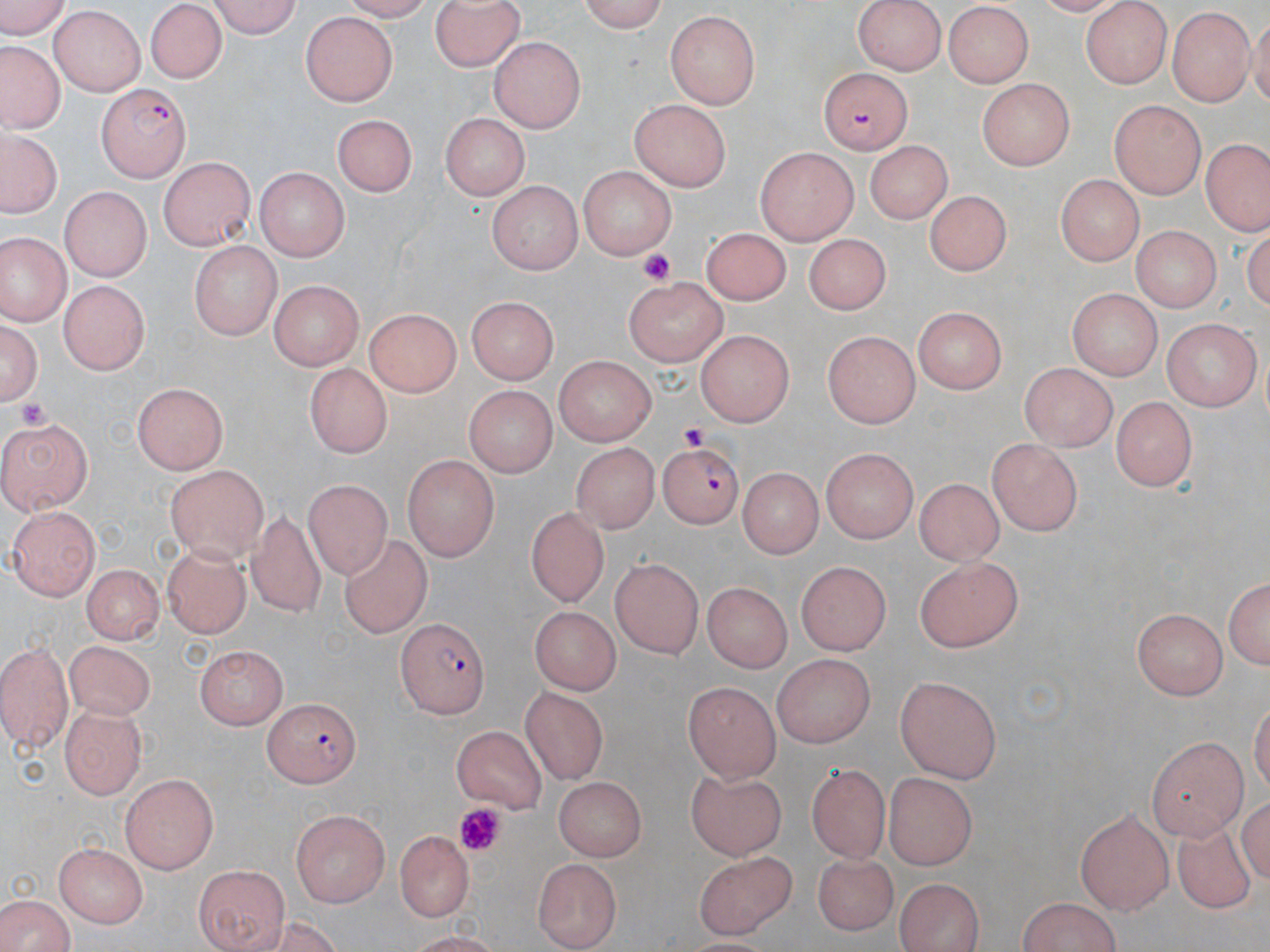
Approximate bounding boxes as (x1,y1)-(x2,y2) corner pairs in pixels. Plasmodium falciparum-infected red blood cell locations: (816,66)-(923,159), (96,83)-(191,181), (657,442)-(743,526), (396,618)-(490,716), (263,696)-(360,788). Platelet locations: (635,249)-(676,287), (16,397)-(58,434), (679,424)-(712,453), (452,804)-(509,859). Uninfected red blood cell locations: (0,0)-(77,37), (211,0)-(305,37), (428,0)-(526,70), (576,0)-(672,34), (852,0)-(943,74), (144,3)-(225,83), (1083,3)-(1171,90), (941,4)-(1036,85), (49,8)-(147,96), (1167,8)-(1254,106), (668,10)-(760,109), (299,11)-(403,105), (489,36)-(587,132), (4,47)-(60,130), (978,79)-(1071,170), (628,99)-(733,192), (1111,100)-(1205,197), (333,112)-(420,197), (440,113)-(530,201), (3,130)-(58,217), (1202,135)-(1270,235), (862,140)-(950,225), (756,146)-(858,245), (159,155)-(256,251), (576,164)-(676,259), (251,168)-(348,263), (1056,172)-(1139,264), (488,179)-(580,272), (61,185)-(149,281), (927,192)-(1008,275), (1133,224)-(1219,315), (703,227)-(789,303), (1,233)-(74,324), (801,235)-(891,317), (190,242)-(280,340), (622,276)-(730,362), (60,279)-(148,375), (264,279)-(366,372), (1064,288)-(1165,378), (462,294)-(557,380), (360,300)-(458,398), (910,309)-(1005,395), (1,318)-(41,407), (1159,318)-(1261,408), (695,332)-(796,428), (821,332)-(922,427), (550,356)-(658,443), (1017,360)-(1118,449), (303,364)-(398,454), (130,384)-(231,472), (462,386)-(557,475), (1106,398)-(1198,492), (0,414)-(96,514), (986,436)-(1082,537), (572,444)-(655,536), (820,448)-(917,542), (402,454)-(499,559), (166,464)-(270,559), (742,468)-(822,559), (916,477)-(1004,566), (302,480)-(398,583), (524,504)-(609,606), (243,505)-(328,619), (6,507)-(102,598), (337,534)-(432,636), (161,544)-(253,635), (916,554)-(1026,650), (611,557)-(705,659), (798,561)-(892,655), (80,562)-(167,642), (1224,573)-(1270,675), (700,582)-(795,674), (531,608)-(620,692), (1130,610)-(1228,701), (0,640)-(72,749), (67,640)-(155,720), (195,647)-(287,729), (771,653)-(877,745), (895,674)-(1004,781), (683,678)-(777,778), (523,685)-(606,785), (59,706)-(145,798), (451,724)-(545,812), (1146,734)-(1248,836), (806,762)-(888,858), (884,772)-(974,870), (120,773)-(220,872), (556,777)-(646,858), (83,781)-(212,917), (289,807)-(392,903), (1075,808)-(1175,912), (1173,815)-(1257,919), (392,829)-(476,921), (55,840)-(147,928), (693,847)-(799,940), (809,853)-(896,932), (530,857)-(623,947), (195,864)-(288,950), (893,877)-(983,952), (0,896)-(81,952), (1015,899)-(1128,952). Slide-level diagnosis: Plasmodium falciparum. Optical microscopy. Single field of view. 1000x magnification. Image is 1270×952 pixels. Thin blood film. May-Grünwald-Giemsa-stained preparation.